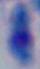

identification = Toxoplasma gondii
modality = photomicrograph
magnification = 1000x